Name the blood parasite species.
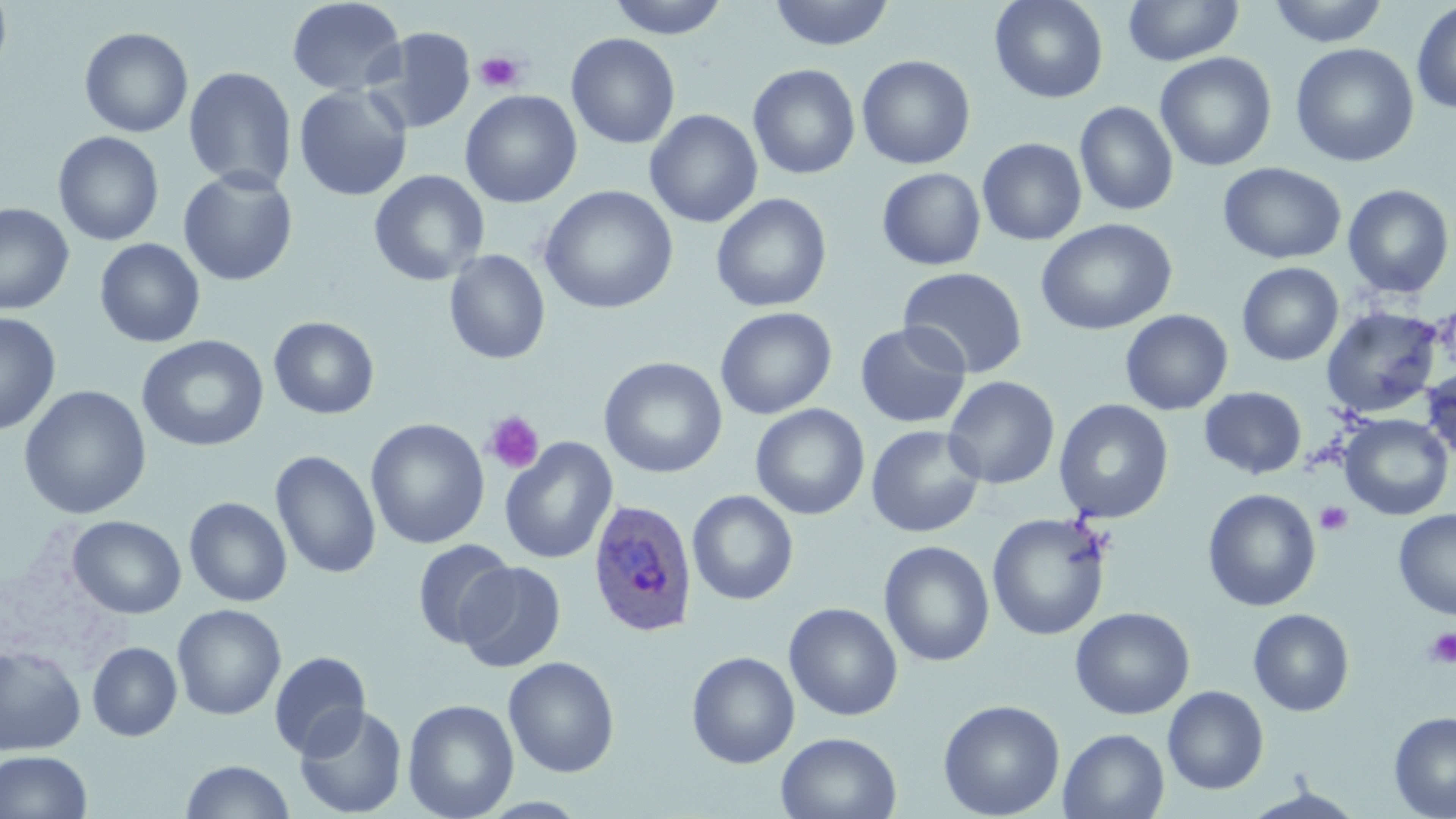
Plasmodium ovale.

{
  "stain": "May-Grünwald-Giemsa",
  "preparation": "thin blood film",
  "plasmodium_ovale_infected_red_blood_cell_locations": "approximate bounding boxes as (x1, y1, x2, y2) in pixels: (587, 498, 698, 638)",
  "image_size": "1456×819 pixels",
  "platelet_locations": "approximate bounding boxes as (x1, y1, x2, y2) in pixels: (473, 51, 524, 93), (482, 411, 544, 474), (1315, 501, 1354, 535), (1423, 627, 1456, 668)",
  "modality": "light microscopy",
  "magnification": "1000x",
  "uninfected_red_blood_cell_locations": "approximate bounding boxes as (x1, y1, x2, y2) in pixels: (0, 0, 13, 83), (286, 0, 406, 97), (607, 0, 729, 39), (768, 0, 895, 51), (990, 0, 1108, 103), (1123, 0, 1243, 66), (1266, 0, 1390, 46), (1411, 1, 1456, 114), (366, 26, 476, 134), (79, 27, 193, 138), (566, 33, 681, 149), (1290, 43, 1420, 167), (1155, 52, 1276, 171), (856, 54, 976, 170), (748, 63, 860, 180), (183, 66, 298, 194), (293, 84, 413, 202), (460, 89, 582, 208), (1075, 101, 1178, 216), (645, 109, 763, 228), (53, 131, 164, 246), (977, 137, 1087, 245), (1218, 162, 1346, 264), (877, 167, 986, 270), (178, 169, 298, 286), (369, 169, 490, 286), (1342, 184, 1454, 299), (539, 185, 679, 315), (711, 192, 832, 313), (0, 203, 74, 315), (1036, 218, 1177, 336), (95, 238, 205, 348), (443, 249, 551, 364), (1237, 262, 1344, 366), (898, 266, 1028, 379), (1321, 305, 1443, 418), (715, 306, 837, 419), (1120, 309, 1233, 415), (0, 313, 61, 436), (268, 316, 379, 419), (854, 322, 972, 429), (136, 335, 269, 452), (598, 356, 728, 479), (1421, 366, 1456, 463), (943, 375, 1060, 489), (18, 385, 152, 519), (1199, 386, 1307, 480), (1053, 398, 1174, 524), (750, 403, 870, 520), (1339, 414, 1453, 520), (365, 418, 490, 549), (866, 424, 986, 538), (499, 437, 617, 565), (270, 450, 381, 579), (1202, 488, 1321, 612), (687, 490, 799, 605), (184, 496, 292, 607), (1393, 509, 1456, 620), (987, 512, 1112, 641), (67, 515, 186, 618), (411, 539, 516, 650), (878, 540, 995, 667), (456, 561, 567, 672), (783, 602, 903, 721), (172, 604, 287, 720), (1070, 606, 1194, 719), (1248, 608, 1355, 716), (87, 642, 182, 741), (0, 646, 86, 756), (268, 650, 371, 759), (686, 651, 800, 769), (503, 656, 620, 777), (1163, 686, 1269, 795), (402, 698, 519, 819), (938, 699, 1065, 819), (295, 703, 407, 818), (1389, 710, 1456, 819), (1059, 728, 1169, 819), (776, 731, 901, 819), (0, 750, 93, 819), (180, 760, 295, 818), (1241, 787, 1367, 819)",
  "field_of_view": "one of a larger specimen"
}